Assess this cell for malaria.
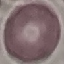

Uninfected.

Automatically extracted cell patch, resized to 64 × 64 pixels. Giemsa-stained preparation. Thin smear of blood. Acquired by smartphone through the microscope eyepiece.